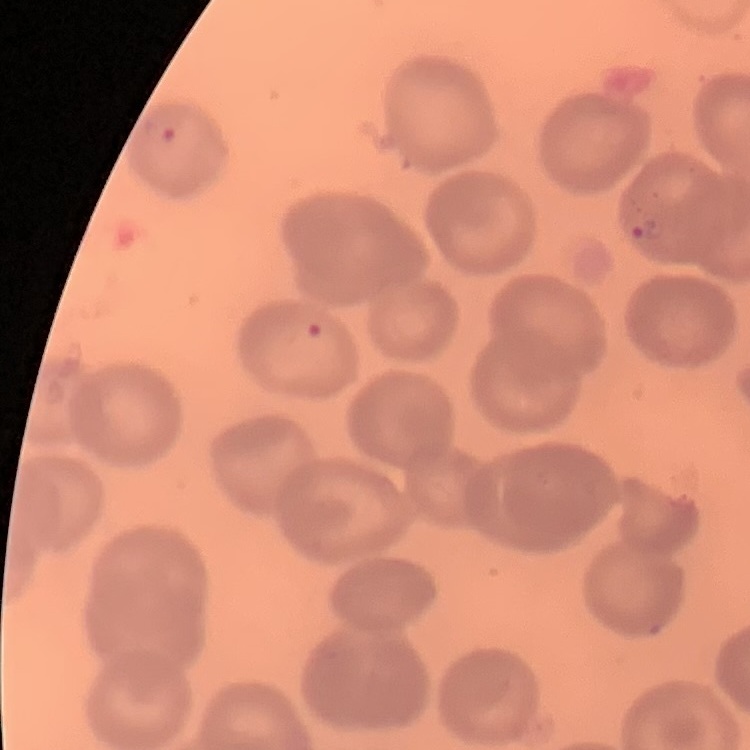 The red blood cells exhibit no rouleaux formation. Thin blood smear. Stained with either Field's or Giemsa. One tile cut from a larger photomicrograph.